Locate every Plasmodium parasite.
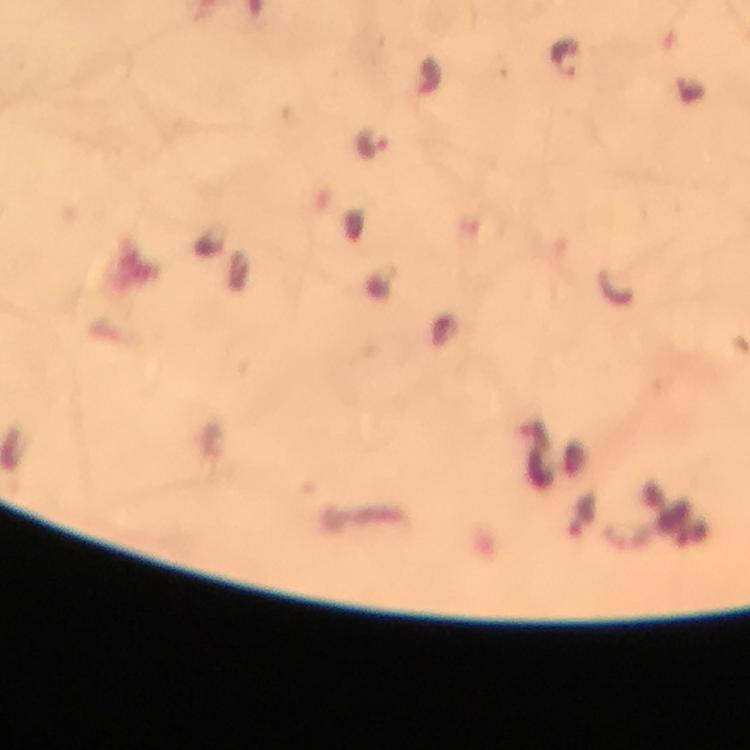

Approximate centers as [x, y] in pixels.
Plasmodium parasites: [565, 60], [373, 144].

Summary:
  - Stain: Giemsa
  - Capture: smartphone photograph through a microscope
  - Context: from a diagnostic examination for malaria
  - Image size: 750×750 pixels
  - Immersion oil: used
  - Cropped from: a single field of view
  - Preparation: thick smear
  - Magnification: 100x